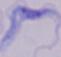

Photomicrograph. Captured at 1000x magnification. A trypanosome is seen.